Name the parasite shown.
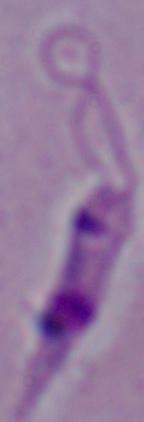
Leishmania.

Micrograph. Captured at 1000x magnification.